Identify the parasite.
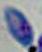

This is Toxoplasma gondii.

magnification = 1000x
modality = photomicrograph